Name the blood parasite species.
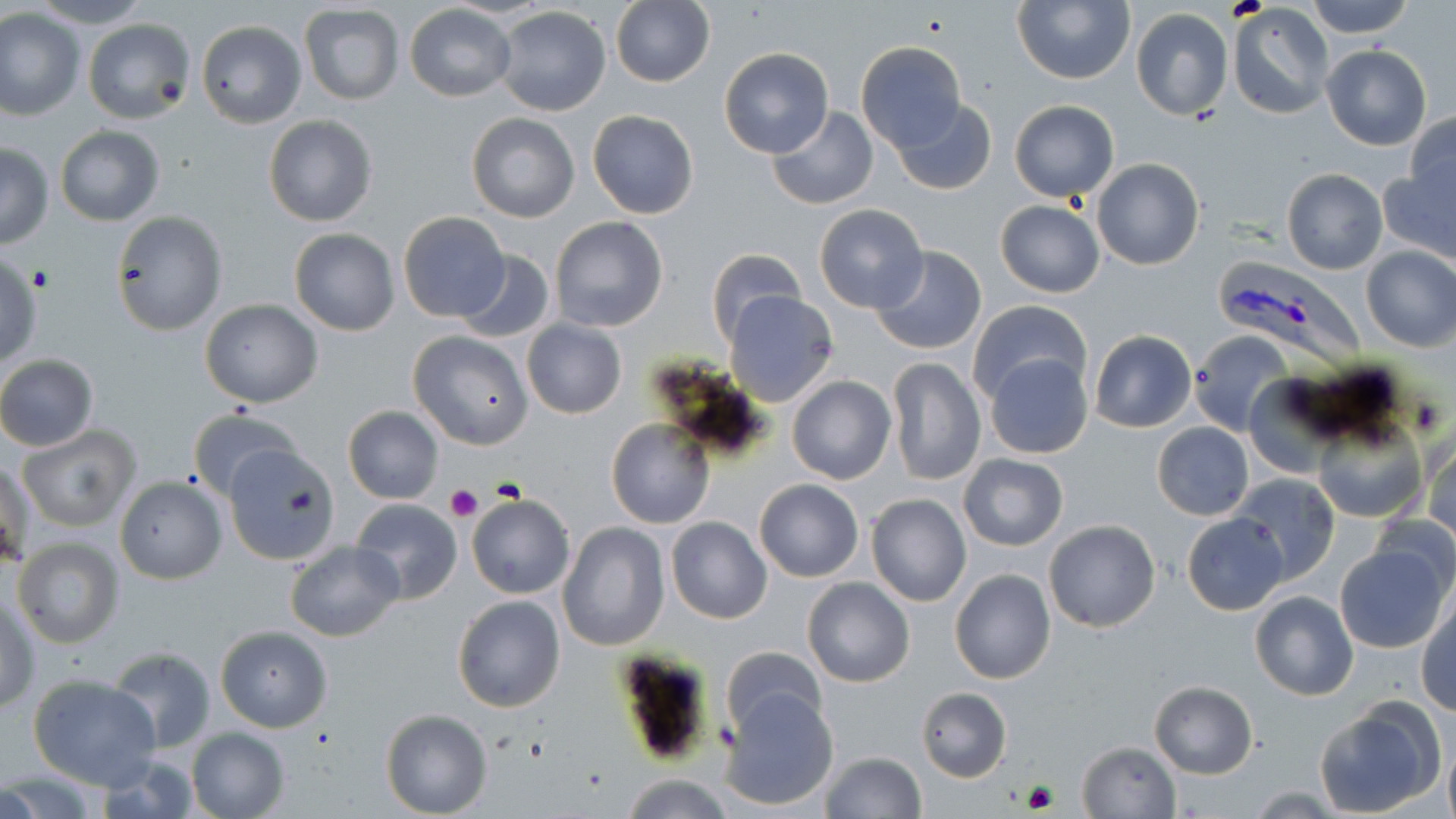

Plasmodium vivax.

Approximate bounding boxes as (x1,y1)-(x2,y2) corner pairs in pixels. Platelet locations: (28,265)-(58,294), (445,484)-(483,521), (1023,779)-(1059,813). Plasmodium vivax-infected red blood cell locations: (1214,257)-(1371,370). Uninfected red blood cell locations: (32,0)-(152,28), (1306,0)-(1414,38), (611,1)-(716,88), (1012,1)-(1135,85), (299,4)-(405,105), (404,4)-(516,103), (1228,4)-(1334,119), (493,5)-(612,116), (1130,7)-(1234,122), (0,9)-(86,121), (82,18)-(195,124), (196,20)-(306,129), (855,41)-(966,149), (1322,44)-(1432,150), (719,48)-(833,158), (890,100)-(998,197), (1009,100)-(1119,200), (766,107)-(879,210), (587,110)-(699,219), (465,112)-(579,223), (1404,112)-(1456,206), (263,114)-(379,226), (56,125)-(164,225), (0,144)-(53,249), (1091,158)-(1205,270), (1378,165)-(1456,262), (1281,168)-(1387,275), (995,201)-(1106,298), (812,204)-(929,313), (111,210)-(227,335), (399,211)-(510,322), (550,216)-(668,331), (289,227)-(400,336), (869,245)-(987,355), (1360,246)-(1455,352), (703,248)-(807,349), (453,250)-(554,344), (0,255)-(42,369), (724,292)-(838,406), (199,299)-(324,407), (968,300)-(1091,409), (520,319)-(628,420), (1189,329)-(1297,438), (407,330)-(533,449), (1088,330)-(1196,433), (984,351)-(1093,459), (0,354)-(99,451), (886,358)-(986,486), (1242,375)-(1339,477), (787,376)-(895,485), (343,405)-(444,504), (187,409)-(306,503), (1313,416)-(1426,522), (606,417)-(714,529), (1152,422)-(1253,520), (1162,423)-(1263,610), (19,425)-(141,532), (1423,434)-(1456,542), (226,444)-(342,564), (2,452)-(33,568), (958,455)-(1068,551), (1230,474)-(1340,586), (114,475)-(227,583), (754,479)-(863,582), (866,493)-(971,607), (465,494)-(575,599), (351,499)-(463,603), (1368,511)-(1456,600), (1181,512)-(1290,616), (666,516)-(773,624), (556,520)-(670,652), (1044,520)-(1160,633), (12,538)-(124,650), (285,541)-(404,640), (1334,544)-(1449,654), (949,568)-(1056,684), (802,577)-(915,686), (1250,590)-(1359,701), (452,595)-(565,713), (2,596)-(39,712), (1416,603)-(1456,716), (215,625)-(333,732), (720,646)-(827,741), (106,647)-(217,752), (607,650)-(726,768), (28,675)-(161,790), (1150,682)-(1257,777), (717,684)-(838,811), (917,687)-(1012,781), (1312,704)-(1441,816), (380,709)-(492,817), (185,727)-(290,818), (1076,740)-(1180,818), (1443,743)-(1456,819), (819,752)-(926,819), (1,770)-(101,818), (620,774)-(736,817). 1000x magnification. May-Grünwald-Giemsa stain. One field of a larger specimen. Optical microscopy. Thin blood smear. Image is 1456×819 pixels.